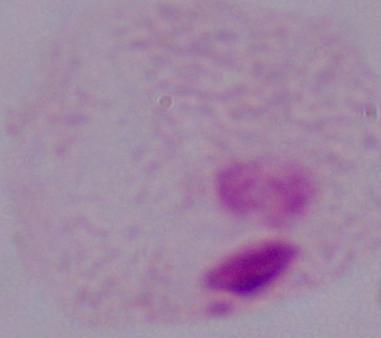 A trichomonad is seen. 1000x magnification. Photomicrograph.